Locate every parasitized red blood cell.
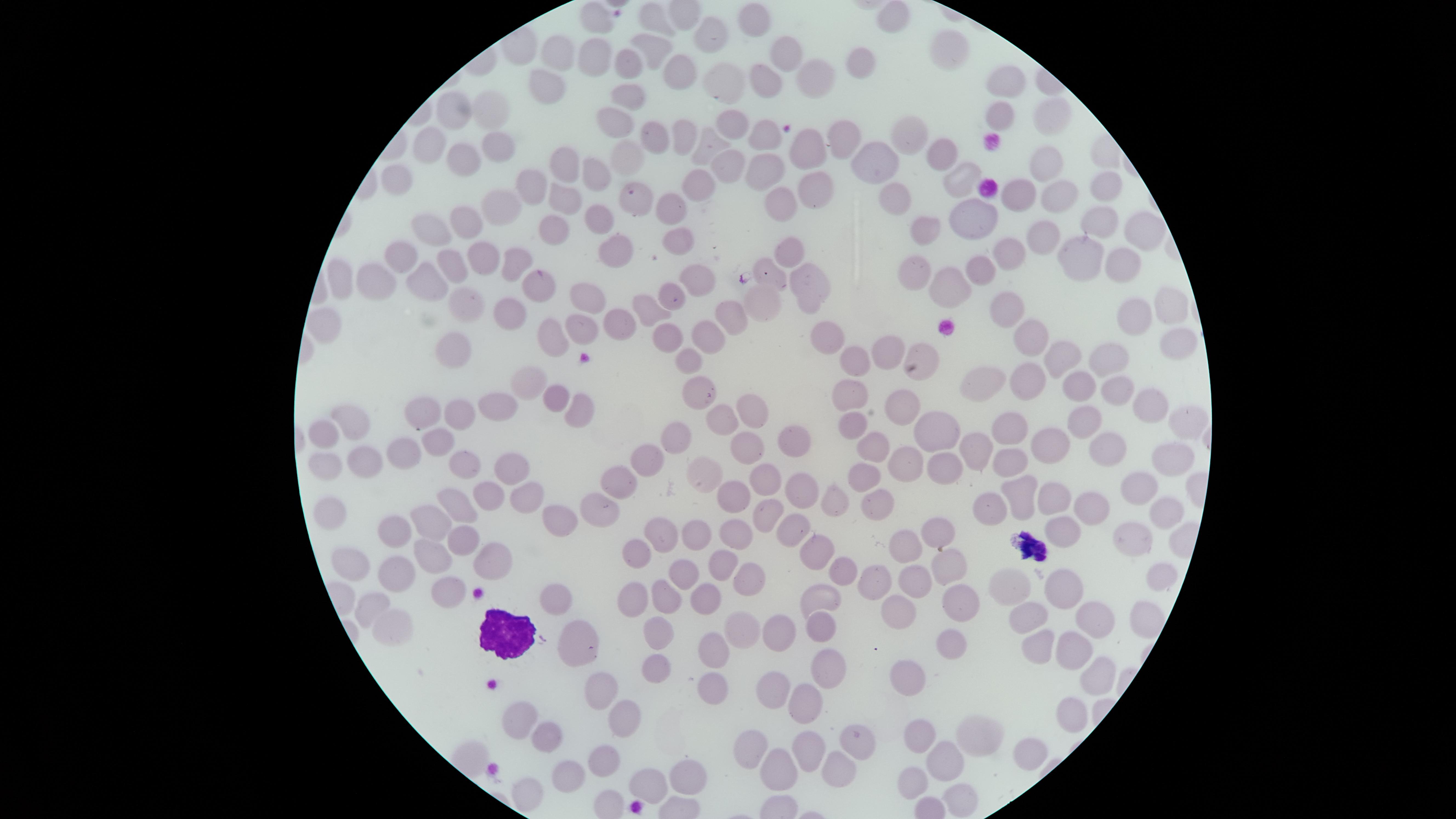

No parasitized red blood cells identified.

Approximate marker points, in pixels from the top-left corner.
Summary:
  - Uninfected red blood cells: (x=596, y=17), (x=892, y=17), (x=655, y=21), (x=754, y=21), (x=718, y=34), (x=946, y=52), (x=657, y=53), (x=554, y=55), (x=596, y=56), (x=788, y=58), (x=863, y=64), (x=633, y=69), (x=677, y=71), (x=817, y=76), (x=729, y=81), (x=769, y=82), (x=1009, y=82), (x=548, y=83), (x=633, y=94), (x=455, y=111), (x=493, y=111), (x=996, y=116), (x=620, y=120), (x=1049, y=120), (x=735, y=127), (x=657, y=131), (x=684, y=132), (x=832, y=136), (x=908, y=137), (x=766, y=140), (x=430, y=145), (x=715, y=145), (x=495, y=146), (x=808, y=153), (x=945, y=156), (x=466, y=159), (x=630, y=160), (x=876, y=164), (x=1047, y=164), (x=565, y=165), (x=768, y=165), (x=728, y=168), (x=597, y=177), (x=404, y=178), (x=965, y=178), (x=706, y=184), (x=813, y=184), (x=530, y=186), (x=1098, y=188), (x=1021, y=191), (x=636, y=194), (x=1058, y=194), (x=568, y=195), (x=895, y=195), (x=783, y=199), (x=670, y=204), (x=505, y=211), (x=597, y=217), (x=975, y=218), (x=1097, y=219), (x=466, y=224), (x=553, y=230), (x=923, y=230), (x=441, y=232), (x=1138, y=233), (x=1044, y=234), (x=677, y=240), (x=618, y=246), (x=1009, y=249), (x=788, y=253), (x=410, y=256), (x=1120, y=256), (x=1080, y=257), (x=508, y=258), (x=451, y=266), (x=482, y=267), (x=980, y=267), (x=341, y=274), (x=911, y=275), (x=772, y=278), (x=535, y=280), (x=693, y=280), (x=379, y=281), (x=804, y=284), (x=943, y=287), (x=429, y=288), (x=670, y=297), (x=586, y=301), (x=765, y=302), (x=1162, y=304), (x=471, y=307), (x=646, y=311), (x=1009, y=311), (x=1136, y=312), (x=508, y=314), (x=733, y=315), (x=618, y=320), (x=586, y=326), (x=715, y=332), (x=1026, y=334), (x=669, y=335), (x=826, y=336), (x=551, y=337), (x=1175, y=344), (x=459, y=351), (x=925, y=351), (x=1060, y=353), (x=891, y=354), (x=693, y=356), (x=853, y=357), (x=1112, y=360), (x=1026, y=384), (x=527, y=386), (x=989, y=386), (x=705, y=387), (x=1080, y=387), (x=1117, y=393), (x=848, y=395), (x=555, y=396), (x=496, y=408), (x=573, y=409), (x=749, y=409), (x=1147, y=409), (x=418, y=410), (x=459, y=410), (x=902, y=411), (x=351, y=416), (x=727, y=418), (x=1187, y=419), (x=1013, y=420), (x=852, y=423), (x=1083, y=423), (x=325, y=432), (x=785, y=434), (x=940, y=435), (x=1049, y=438), (x=680, y=440), (x=870, y=440), (x=1108, y=442), (x=437, y=444), (x=744, y=446), (x=979, y=447), (x=401, y=453), (x=1173, y=454), (x=651, y=459), (x=1014, y=461), (x=361, y=464), (x=462, y=464), (x=904, y=466), (x=938, y=466), (x=327, y=469), (x=504, y=469), (x=867, y=474), (x=623, y=475), (x=702, y=476), (x=766, y=482), (x=1137, y=487), (x=1025, y=490), (x=487, y=492), (x=525, y=495), (x=734, y=495), (x=805, y=495), (x=1061, y=501), (x=990, y=503), (x=602, y=504), (x=831, y=504), (x=874, y=504), (x=1091, y=504), (x=457, y=506), (x=337, y=513), (x=557, y=513), (x=1157, y=516), (x=431, y=518), (x=765, y=518), (x=784, y=529), (x=938, y=531), (x=390, y=532), (x=693, y=532), (x=733, y=535), (x=662, y=536), (x=1060, y=537), (x=1125, y=539), (x=462, y=540), (x=901, y=548), (x=631, y=549), (x=813, y=549), (x=436, y=553), (x=484, y=556), (x=359, y=560), (x=722, y=563), (x=945, y=566), (x=397, y=571), (x=677, y=572), (x=833, y=572), (x=1152, y=577), (x=912, y=578), (x=878, y=582), (x=743, y=583), (x=1011, y=584), (x=1057, y=584), (x=447, y=593), (x=626, y=596), (x=548, y=597), (x=703, y=597), (x=819, y=597), (x=951, y=600), (x=663, y=601), (x=373, y=603), (x=898, y=606), (x=1034, y=614), (x=1090, y=618), (x=391, y=621), (x=818, y=623), (x=734, y=631), (x=774, y=631), (x=661, y=637), (x=573, y=641), (x=951, y=646), (x=1045, y=646), (x=1074, y=646), (x=710, y=650), (x=655, y=671), (x=823, y=671), (x=1096, y=673), (x=905, y=675), (x=769, y=685), (x=597, y=690), (x=710, y=691), (x=801, y=700), (x=1068, y=717), (x=520, y=719), (x=625, y=724), (x=918, y=734), (x=971, y=736), (x=537, y=742), (x=844, y=744), (x=748, y=745), (x=798, y=746), (x=1025, y=749), (x=936, y=754), (x=597, y=764), (x=832, y=769), (x=775, y=770), (x=564, y=776), (x=685, y=777), (x=914, y=781), (x=651, y=782), (x=525, y=793), (x=960, y=800)
  - White blood cells: (x=502, y=634)
  - Preparation: thin smear of blood
  - Capture: smartphone photograph through the microscope eyepiece
  - Image size: 1456×819 pixels
  - Stain: Giemsa
  - Field of view: single
  - Visible region: circular